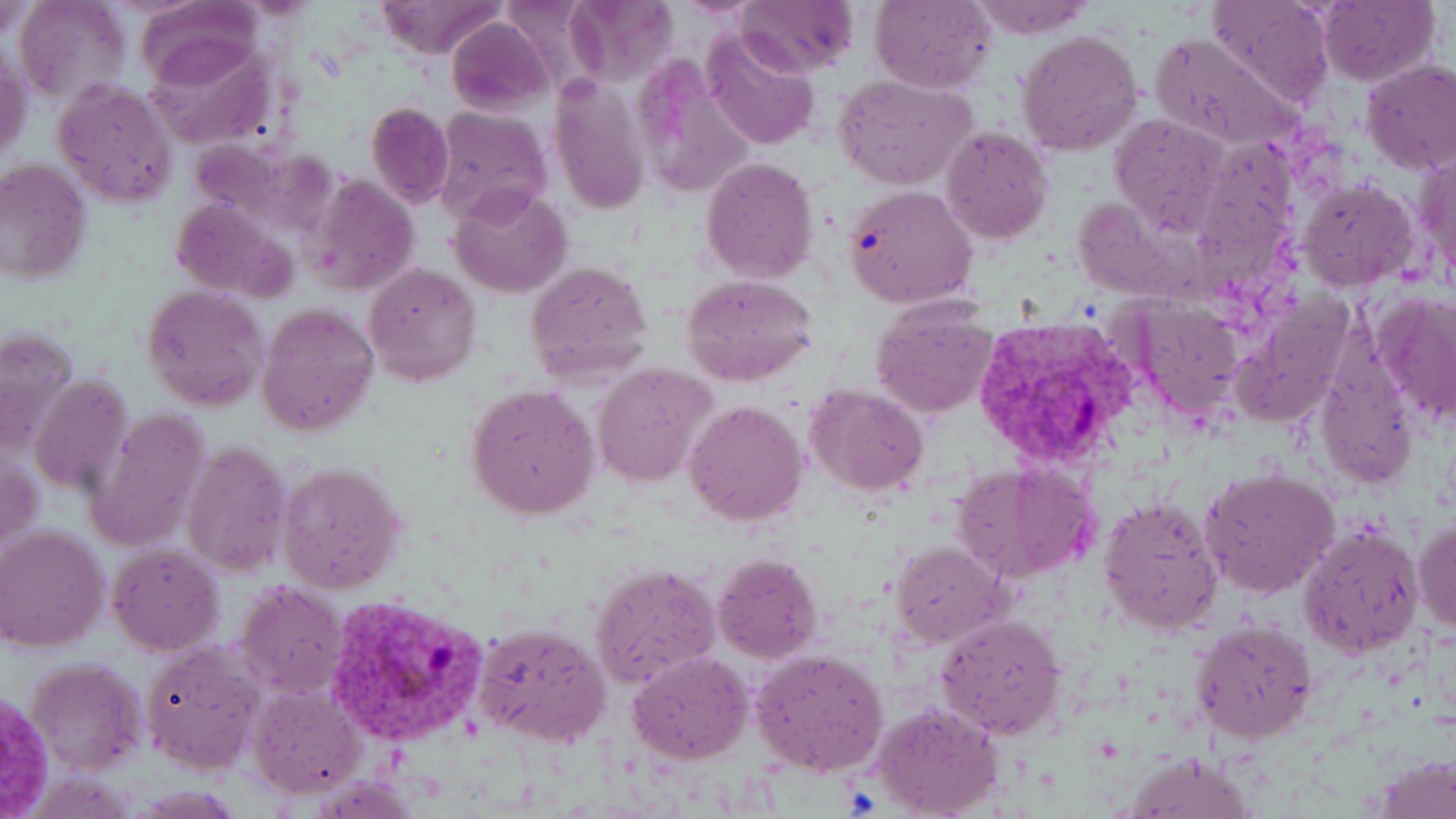
Approximate bounding boxes as named x1/y1/x2/y2 corners in pixels. Uninfected red blood cell locations: (x1=15, y1=0, x2=131, y2=108), (x1=733, y1=0, x2=858, y2=77), (x1=870, y1=0, x2=994, y2=94), (x1=964, y1=0, x2=1093, y2=39), (x1=1207, y1=0, x2=1335, y2=104), (x1=1317, y1=0, x2=1437, y2=85), (x1=132, y1=1, x2=267, y2=91), (x1=375, y1=1, x2=507, y2=60), (x1=563, y1=1, x2=679, y2=82), (x1=0, y1=3, x2=38, y2=44), (x1=447, y1=17, x2=553, y2=117), (x1=1018, y1=29, x2=1143, y2=156), (x1=700, y1=30, x2=820, y2=150), (x1=1148, y1=33, x2=1300, y2=150), (x1=142, y1=37, x2=276, y2=148), (x1=1, y1=42, x2=31, y2=162), (x1=1361, y1=61, x2=1456, y2=176), (x1=834, y1=75, x2=976, y2=189), (x1=550, y1=76, x2=649, y2=216), (x1=52, y1=78, x2=180, y2=209), (x1=366, y1=102, x2=454, y2=206), (x1=433, y1=107, x2=552, y2=229), (x1=1109, y1=114, x2=1230, y2=236), (x1=941, y1=127, x2=1053, y2=243), (x1=1196, y1=138, x2=1302, y2=290), (x1=1409, y1=147, x2=1456, y2=287), (x1=700, y1=156, x2=818, y2=284), (x1=0, y1=160, x2=91, y2=284), (x1=304, y1=173, x2=420, y2=295), (x1=1296, y1=176, x2=1420, y2=292), (x1=450, y1=185, x2=572, y2=298), (x1=843, y1=185, x2=978, y2=309), (x1=1071, y1=198, x2=1187, y2=301), (x1=170, y1=201, x2=294, y2=299), (x1=526, y1=259, x2=655, y2=385), (x1=365, y1=263, x2=481, y2=387), (x1=682, y1=274, x2=820, y2=387), (x1=142, y1=284, x2=270, y2=412), (x1=1372, y1=291, x2=1456, y2=425), (x1=1123, y1=297, x2=1245, y2=422), (x1=870, y1=302, x2=998, y2=417), (x1=256, y1=303, x2=379, y2=438), (x1=0, y1=326, x2=80, y2=451), (x1=590, y1=363, x2=715, y2=488), (x1=29, y1=374, x2=131, y2=495), (x1=805, y1=383, x2=929, y2=495), (x1=466, y1=384, x2=600, y2=520), (x1=684, y1=400, x2=807, y2=525), (x1=84, y1=405, x2=213, y2=551), (x1=183, y1=441, x2=292, y2=577), (x1=278, y1=461, x2=406, y2=596), (x1=953, y1=461, x2=1101, y2=584), (x1=1200, y1=467, x2=1339, y2=599), (x1=1098, y1=494, x2=1223, y2=635), (x1=1412, y1=517, x2=1456, y2=633), (x1=1299, y1=522, x2=1424, y2=659), (x1=1, y1=526, x2=108, y2=652), (x1=891, y1=541, x2=1010, y2=648), (x1=108, y1=543, x2=226, y2=657), (x1=713, y1=553, x2=822, y2=663), (x1=590, y1=562, x2=718, y2=688), (x1=233, y1=579, x2=349, y2=700), (x1=935, y1=612, x2=1066, y2=740), (x1=1191, y1=619, x2=1317, y2=743), (x1=471, y1=622, x2=612, y2=748), (x1=142, y1=641, x2=264, y2=776), (x1=750, y1=648, x2=889, y2=777), (x1=627, y1=650, x2=754, y2=764), (x1=24, y1=655, x2=148, y2=778), (x1=248, y1=684, x2=367, y2=797), (x1=870, y1=699, x2=1006, y2=819), (x1=1124, y1=752, x2=1258, y2=818). Plasmodium vivax-infected red blood cell locations: (x1=971, y1=315, x2=1140, y2=467), (x1=325, y1=596, x2=490, y2=746). Slide-level diagnosis: Plasmodium vivax. Captured at 1000x magnification. Image is 1456×819 pixels. Light microscopy. Single field of view. May-Grünwald-Giemsa stain. Thin blood film.